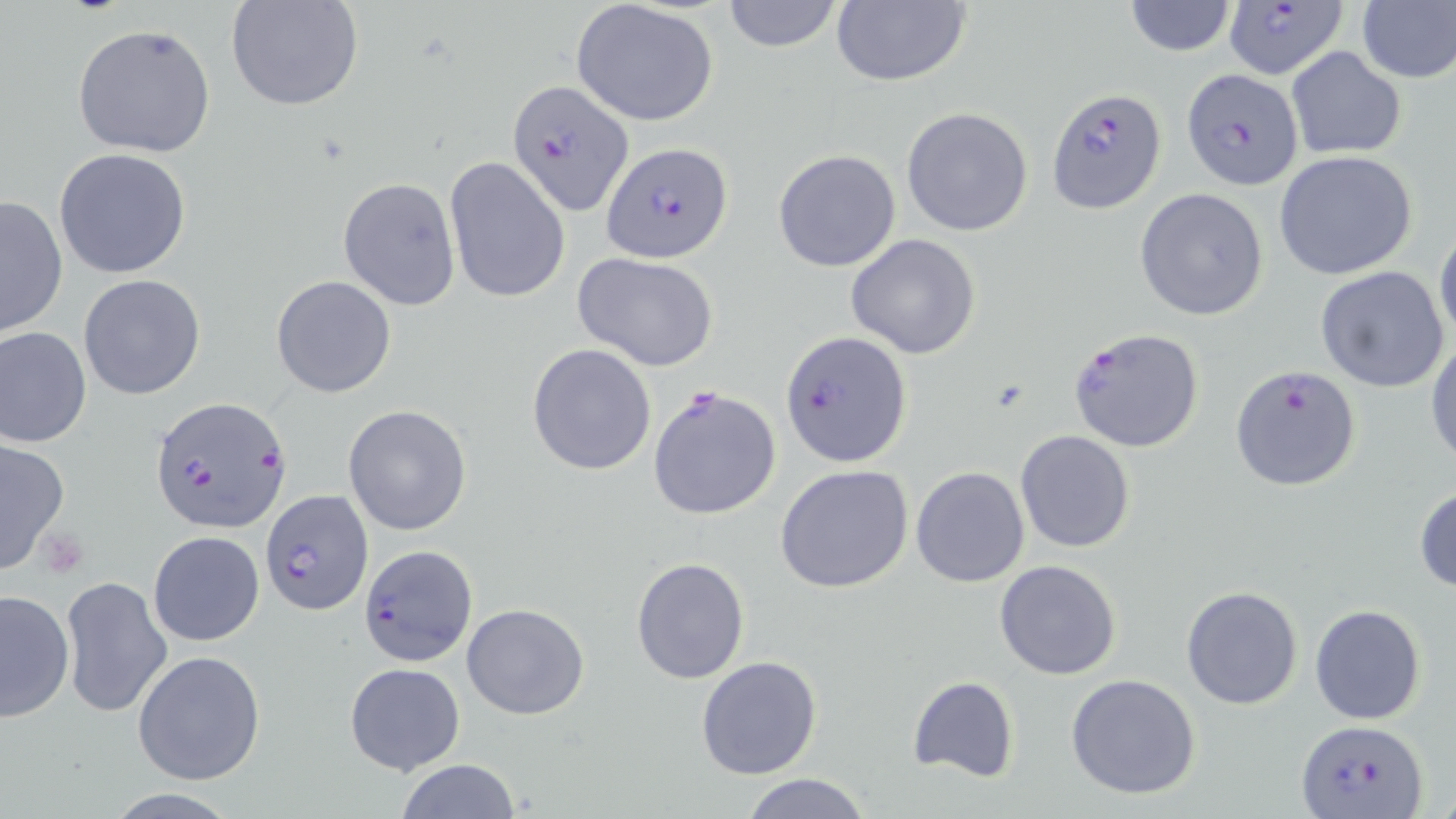
Summary:
  - Coordinate format: approximate bounding boxes as [x1, y1, x2, y2] in pixels
  - Plasmodium falciparum-infected red blood cell locations: [1228, 0, 1351, 79], [1181, 69, 1304, 191], [508, 79, 632, 214], [1046, 87, 1166, 212], [602, 142, 733, 264], [1068, 327, 1205, 453], [781, 330, 911, 468], [1230, 365, 1363, 491], [649, 384, 782, 521], [150, 394, 293, 534], [262, 489, 373, 615], [359, 544, 476, 665], [1297, 718, 1427, 818]
  - Platelet locations: [39, 526, 91, 578]
  - Uninfected red blood cell locations: [226, 0, 366, 112], [720, 0, 845, 51], [830, 0, 972, 87], [1122, 0, 1237, 56], [1356, 0, 1456, 85], [570, 2, 719, 127], [73, 23, 219, 159], [1286, 48, 1406, 161], [901, 107, 1034, 236], [53, 149, 191, 280], [773, 149, 901, 272], [1274, 151, 1421, 282], [444, 155, 571, 305], [337, 176, 461, 310], [1136, 188, 1270, 321], [0, 194, 69, 338], [1434, 226, 1456, 343], [847, 232, 981, 359], [573, 251, 719, 372], [1315, 266, 1451, 394], [78, 273, 206, 401], [271, 274, 397, 398], [0, 326, 93, 448], [1427, 339, 1456, 467], [527, 343, 658, 475], [341, 404, 471, 534], [1014, 429, 1137, 552], [0, 438, 70, 573], [775, 464, 914, 594], [910, 466, 1030, 587], [1413, 483, 1456, 594], [147, 530, 265, 646], [630, 556, 749, 686], [994, 560, 1123, 680], [60, 575, 172, 720], [1181, 585, 1302, 709], [0, 588, 76, 722], [461, 603, 589, 719], [1309, 604, 1427, 725], [133, 650, 266, 785], [696, 655, 822, 778], [344, 662, 465, 776], [1065, 673, 1202, 800], [906, 676, 1019, 783], [393, 759, 521, 819], [740, 773, 872, 818]
  - Slide-level diagnosis: Plasmodium falciparum
  - Stain: May-Grünwald-Giemsa
  - Image size: 1456×819 pixels
  - Preparation: thin blood film
  - Magnification: 1000x
  - Field of view: single
  - Modality: light microscopy